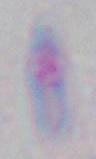
Micrograph. Toxoplasma gondii is seen. 1000x magnification.